Describe the morphology of the red blood cells.
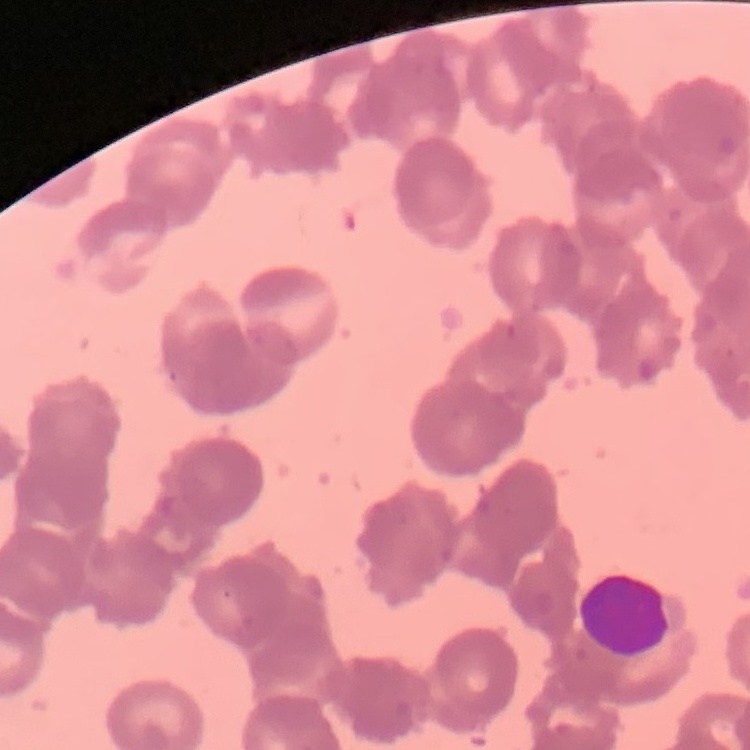

They show rouleaux formation.

stain = Field's or Giemsa
preparation = thin blood smear
image type = square crop of a larger photomicrograph